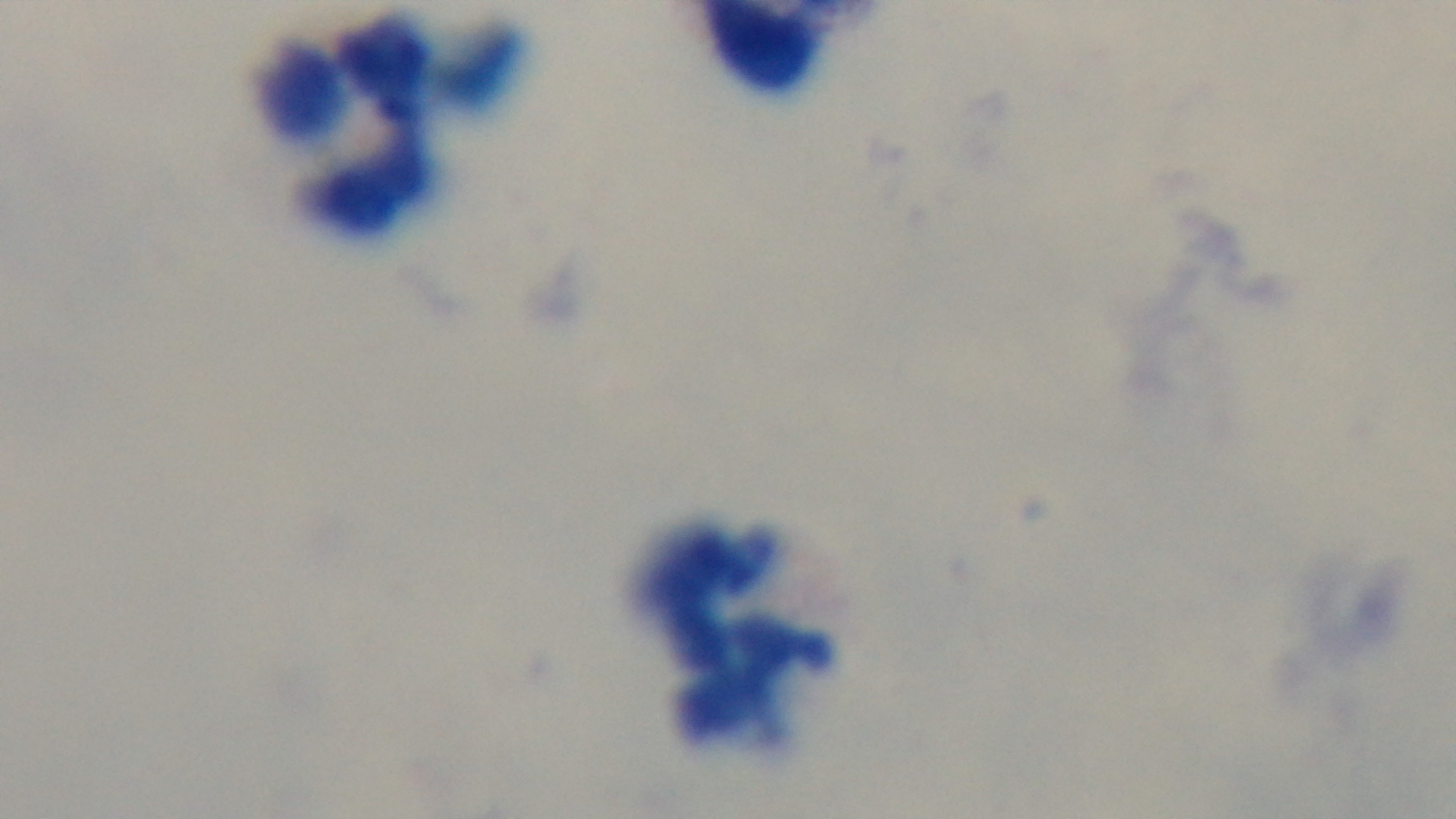

Malaria status: negative. Preparation: thick smear. Photomicrograph. Giemsa-stained. Mounted 4K digital camera. 100x oil-immersion objective. One field from the slide.